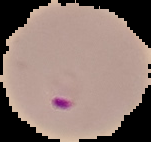

{
  "image_size": "151×142 pixels",
  "preparation": "thin blood film",
  "image_type": "segmented cell region on a black background",
  "result": "malaria parasites identified"
}